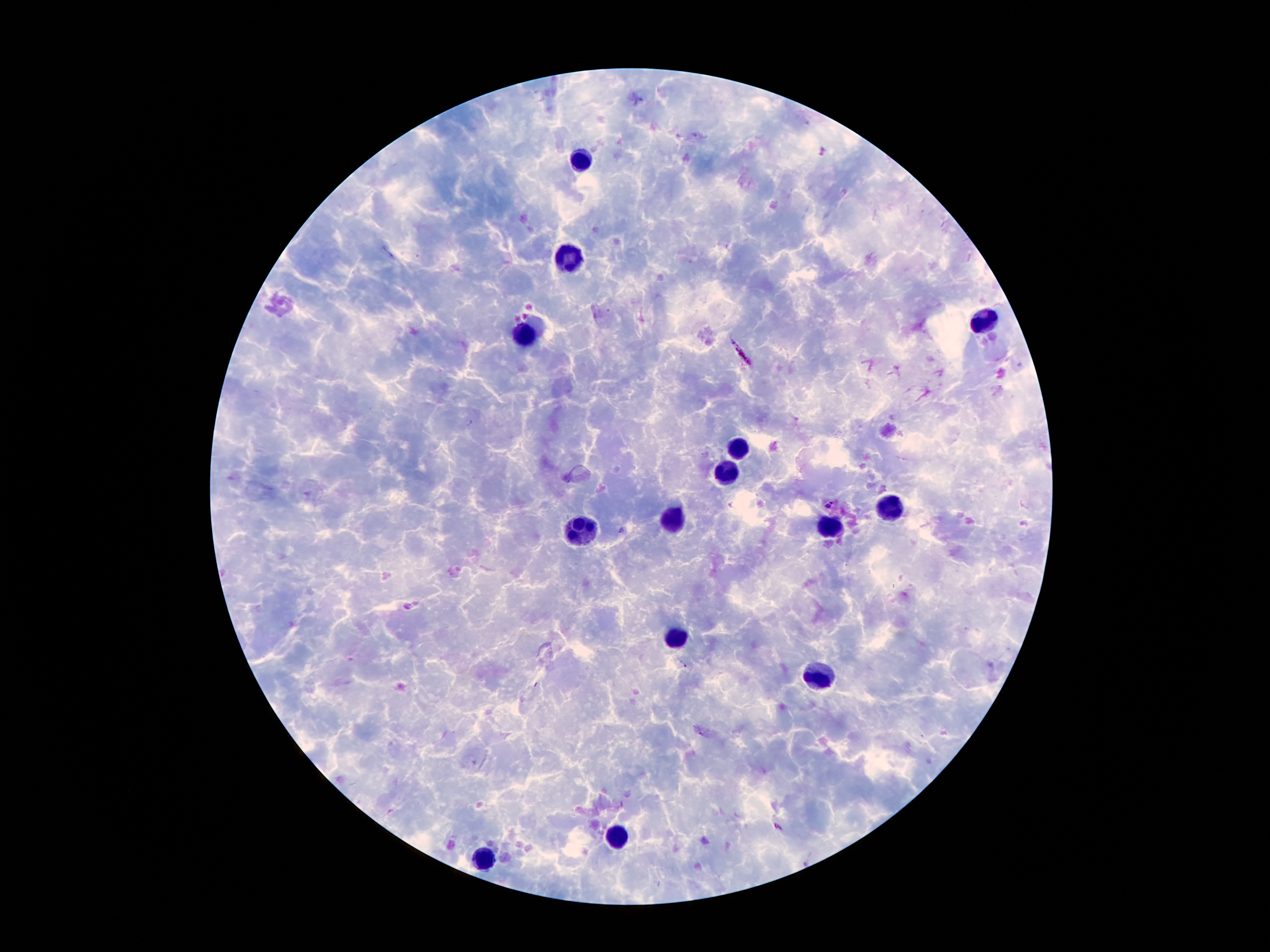
Approximate centers as {x, y} in pixels. Leukocyte locations: {582, 154}, {569, 257}, {988, 320}, {525, 332}, {739, 448}, {730, 473}, {886, 509}, {680, 518}, {830, 527}, {582, 529}, {675, 634}, {821, 675}, {616, 834}, {482, 857}. Malaria parasite locations: {742, 353}, {830, 505}. Giemsa-stained preparation. Photographed through the microscope eyepiece with a smartphone camera. 100x magnification. One field from this slide. Patient malaria status: infected with Plasmodium falciparum. Thick peripheral-blood smear. Image is 1270×952 pixels.